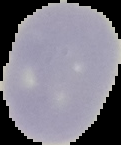

preparation = thin blood smear
result = no Plasmodium parasites seen
image type = segmented cell region with the area outside set to black
image size = 121×145 pixels